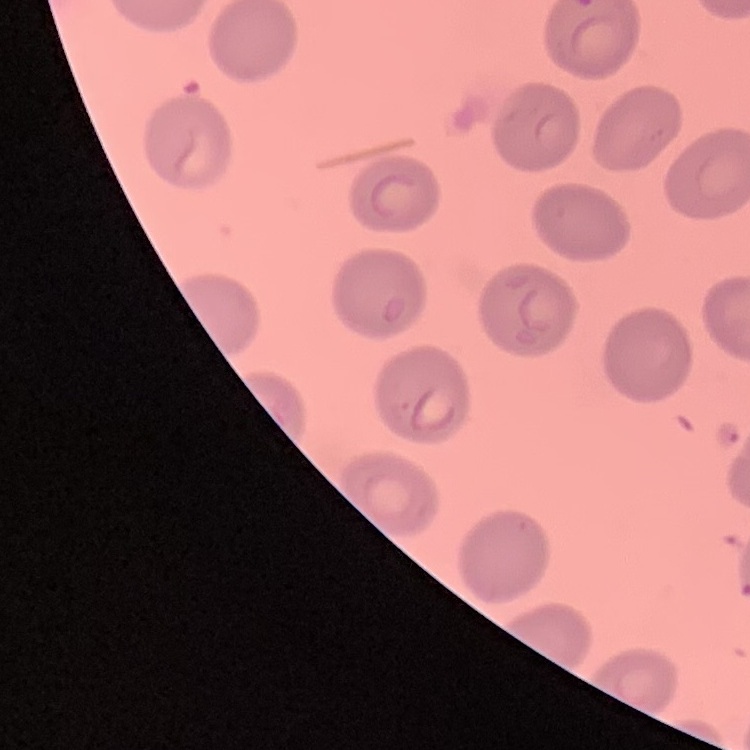
{
  "erythrocyte_morphology": "no rouleaux formation",
  "preparation": "thin peripheral smear",
  "stain": "Field's or Giemsa",
  "image_type": "square crop of a larger photomicrograph"
}